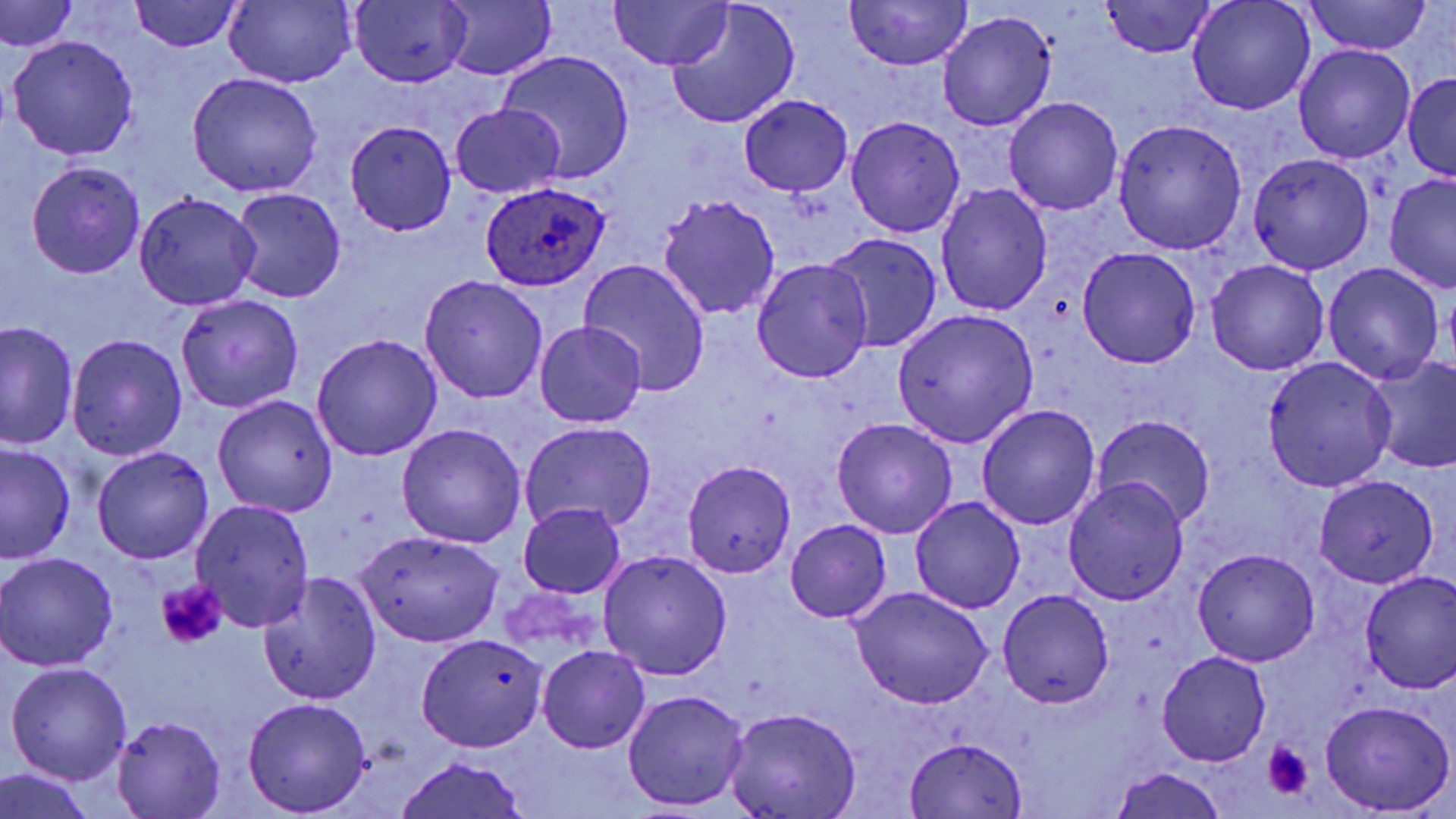

Summary:
  - Coordinate format: approximate bounding boxes as [x1, y1, x2, y2] in pixels
  - Uninfected red blood cell locations: [609, 0, 730, 71], [844, 0, 970, 71], [1186, 0, 1317, 117], [1, 1, 78, 54], [129, 1, 242, 52], [224, 1, 354, 87], [1102, 1, 1218, 58], [1303, 1, 1434, 56], [347, 2, 472, 89], [666, 2, 800, 129], [439, 3, 556, 80], [936, 13, 1054, 131], [6, 35, 140, 160], [1293, 46, 1416, 164], [498, 50, 635, 183], [187, 72, 323, 196], [1403, 73, 1456, 179], [740, 94, 853, 197], [1003, 97, 1124, 217], [450, 104, 565, 199], [846, 116, 966, 238], [1113, 119, 1247, 254], [344, 120, 457, 235], [1248, 153, 1374, 276], [26, 160, 145, 278], [1383, 174, 1456, 292], [936, 183, 1053, 317], [229, 187, 346, 304], [133, 193, 260, 310], [657, 196, 782, 320], [826, 233, 942, 354], [1076, 246, 1201, 369], [579, 258, 713, 396], [751, 258, 875, 383], [1206, 259, 1329, 376], [1323, 264, 1444, 384], [419, 276, 548, 403], [176, 293, 304, 413], [892, 308, 1039, 449], [536, 321, 647, 428], [2, 322, 77, 451], [68, 334, 187, 460], [310, 335, 440, 461], [1263, 355, 1398, 490], [1366, 357, 1456, 476], [212, 394, 338, 518], [976, 404, 1101, 531], [1093, 413, 1216, 529], [831, 417, 958, 538], [520, 421, 657, 534], [396, 423, 526, 548], [0, 444, 75, 564], [91, 447, 214, 564], [682, 459, 796, 577], [1315, 475, 1440, 588], [1064, 478, 1189, 605], [910, 495, 1025, 614], [190, 499, 315, 632], [517, 504, 627, 598], [786, 519, 890, 622], [354, 530, 504, 648], [1193, 547, 1321, 667], [0, 552, 120, 671], [599, 552, 732, 681], [255, 569, 383, 704], [1358, 570, 1456, 693], [849, 587, 992, 709], [998, 589, 1115, 708], [415, 633, 548, 752], [538, 645, 651, 753], [1155, 651, 1272, 766], [5, 662, 132, 784], [622, 688, 749, 811], [242, 697, 373, 815], [1319, 700, 1454, 815], [724, 709, 862, 819], [112, 715, 226, 819], [906, 737, 1029, 817], [393, 756, 531, 819], [1110, 766, 1228, 819], [0, 768, 94, 819]
  - Plasmodium ovale-infected red blood cell locations: [481, 181, 609, 290]
  - Platelet locations: [155, 579, 227, 650], [1262, 743, 1313, 800]
  - Slide-level diagnosis: Plasmodium ovale
  - Image size: 1456×819 pixels
  - Field of view: one of a larger specimen
  - Modality: light microscopy
  - Preparation: thin blood smear
  - Magnification: 1000x
  - Stain: May-Grünwald-Giemsa